State the preparation type.
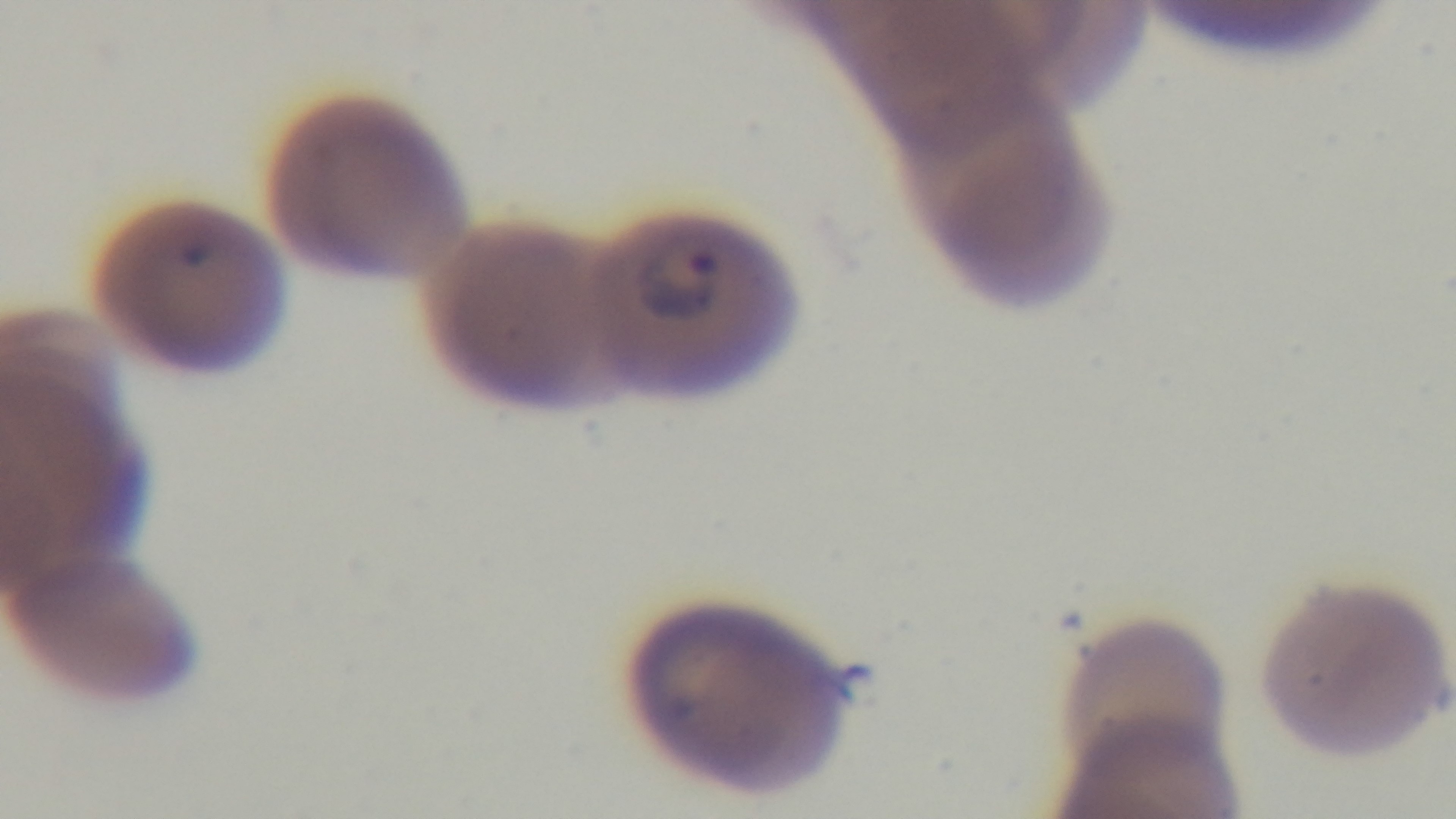

A thin smear.

Giemsa stain. 100x oil-immersion objective. Malaria status: positive. Light microscopy. Captured with a mounted 4K digital camera. Single field of view.